Report the malaria status of this cell.
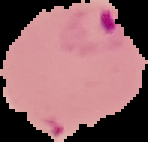
Parasitized.

image size = 148×142 pixels
image type = segmented cell region with the area outside set to black
preparation = thin blood smear